Name the blood parasite species.
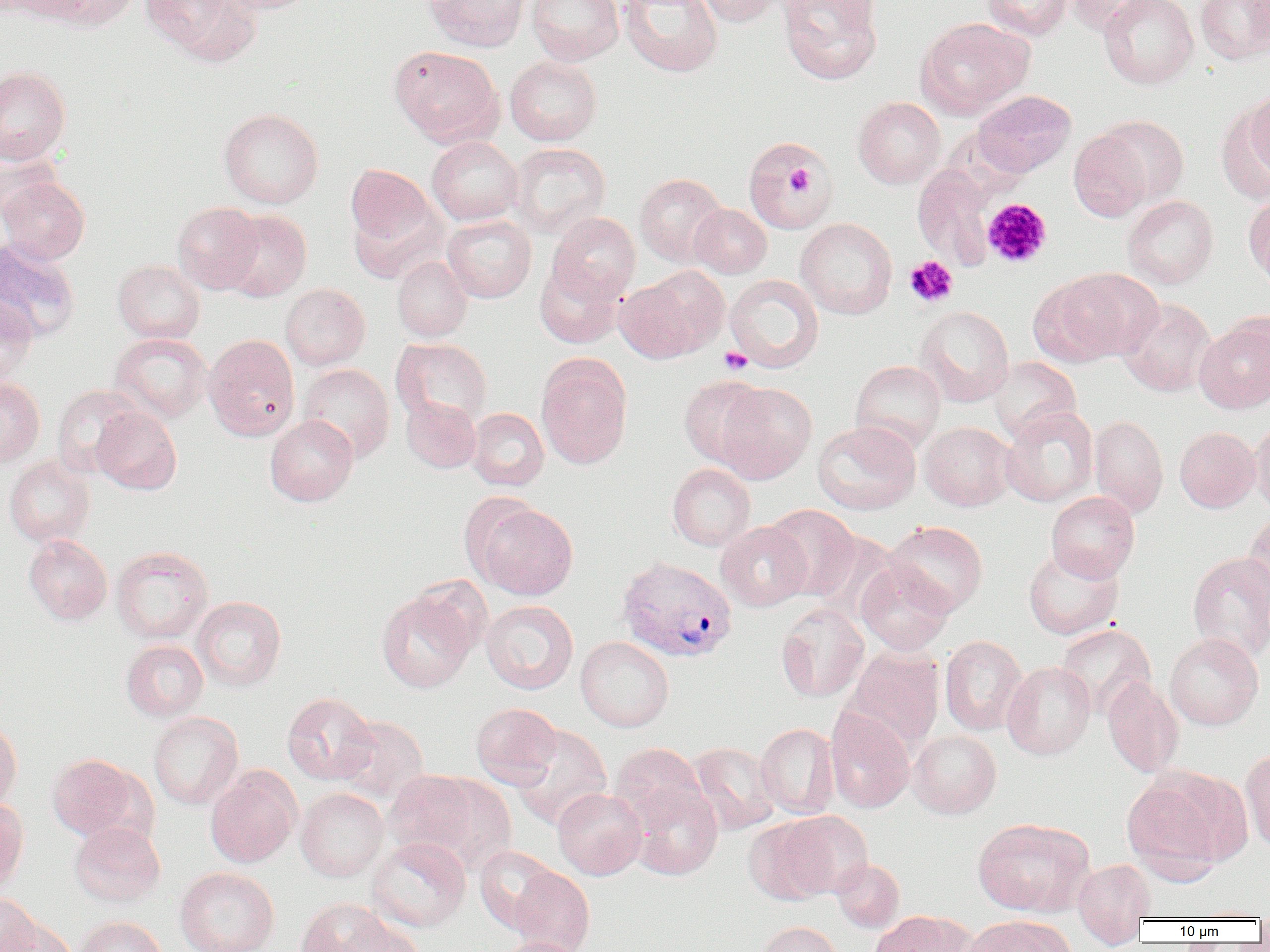

Plasmodium vivax.

Approximate bounding boxes as (x1, y1, x2, y2) in pixels. Plasmodium vivax-infected red blood cell locations: (617, 556, 738, 662). Uninfected red blood cell locations: (3, 0, 90, 23), (49, 0, 137, 31), (143, 0, 259, 63), (214, 0, 320, 15), (424, 0, 529, 52), (526, 0, 623, 65), (620, 0, 723, 77), (693, 0, 781, 27), (778, 0, 883, 85), (982, 0, 1074, 40), (1067, 0, 1156, 36), (1099, 0, 1198, 89), (1195, 0, 1270, 64), (915, 17, 1033, 119), (389, 45, 504, 147), (505, 56, 602, 145), (0, 67, 71, 164), (1244, 88, 1270, 178), (972, 90, 1076, 177), (1222, 96, 1269, 201), (852, 97, 946, 189), (218, 108, 324, 209), (1096, 115, 1189, 205), (1069, 129, 1154, 222), (427, 136, 523, 225), (744, 136, 837, 234), (0, 140, 62, 225), (509, 143, 610, 238), (912, 163, 1000, 270), (345, 164, 436, 251), (635, 173, 728, 266), (0, 176, 90, 264), (1243, 194, 1270, 286), (1122, 195, 1219, 288), (172, 202, 264, 294), (689, 204, 772, 278), (220, 209, 312, 302), (548, 212, 641, 302), (442, 215, 536, 303), (795, 218, 897, 319), (0, 239, 80, 343), (392, 256, 472, 341), (112, 260, 205, 343), (534, 261, 623, 348), (1048, 268, 1163, 363), (614, 274, 713, 364), (724, 274, 824, 372), (280, 283, 370, 370), (0, 296, 38, 385), (1118, 298, 1216, 396), (915, 306, 1015, 406), (1194, 318, 1270, 413), (110, 332, 212, 423), (204, 334, 300, 440), (391, 338, 492, 427), (536, 354, 633, 470), (988, 357, 1081, 442), (850, 360, 946, 452), (298, 364, 395, 463), (679, 375, 771, 467), (0, 377, 44, 466), (715, 382, 817, 483), (51, 385, 143, 477), (401, 397, 481, 473), (92, 406, 182, 494), (1000, 406, 1098, 507), (467, 408, 548, 490), (265, 415, 358, 506), (1089, 415, 1168, 517), (1250, 419, 1270, 516), (812, 421, 921, 515), (919, 422, 1015, 511), (1174, 427, 1261, 512), (4, 455, 95, 548), (668, 464, 755, 551), (1046, 492, 1140, 582), (472, 502, 578, 600), (765, 504, 860, 600), (1244, 513, 1270, 610), (716, 521, 812, 611), (884, 521, 988, 616), (23, 535, 112, 625), (1023, 545, 1124, 639), (111, 546, 214, 643), (1187, 552, 1270, 662), (855, 561, 954, 655), (376, 588, 479, 693), (191, 596, 286, 690), (481, 600, 578, 694), (775, 603, 869, 702), (1056, 624, 1156, 718), (1164, 633, 1264, 730), (575, 636, 674, 732), (940, 636, 1028, 735), (121, 640, 209, 721), (844, 647, 944, 750), (1002, 661, 1095, 760), (1102, 675, 1184, 778), (282, 692, 378, 785), (471, 703, 562, 787), (825, 707, 915, 812), (148, 711, 244, 810), (335, 715, 429, 804), (0, 718, 22, 811), (755, 723, 839, 819), (510, 724, 612, 830), (908, 730, 1001, 818), (610, 742, 706, 826), (688, 742, 781, 835), (1241, 748, 1270, 853), (47, 754, 142, 841), (205, 767, 301, 867), (384, 769, 504, 871), (1121, 771, 1240, 878), (625, 780, 723, 880), (296, 788, 389, 881), (552, 788, 647, 879), (0, 796, 29, 893), (775, 810, 873, 900), (745, 817, 837, 905), (972, 818, 1094, 917), (69, 822, 165, 906), (367, 836, 471, 932), (474, 846, 561, 933), (832, 858, 904, 932), (1072, 858, 1156, 929), (508, 866, 595, 952), (175, 867, 279, 952), (0, 895, 40, 952), (296, 898, 394, 952), (869, 911, 972, 952), (74, 916, 167, 952), (963, 916, 1070, 952), (2, 918, 77, 952), (338, 918, 425, 952), (756, 922, 844, 952), (494, 937, 588, 952). Platelet locations: (787, 164, 816, 196), (982, 198, 1052, 268), (905, 255, 958, 307), (719, 347, 753, 374). 1000x magnification. Image is 1270×952 pixels. Single field of view. Thin blood smear. Light microscopy.